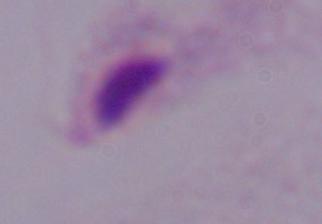

A trichomonad is seen. 1000x magnification. Micrograph.